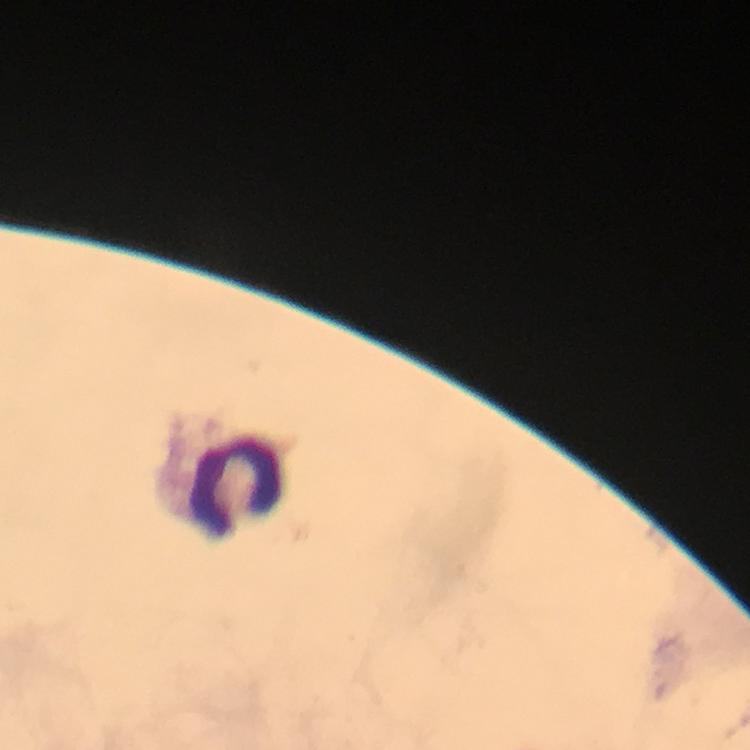
capture: smartphone camera through the microscope
immersion_oil: used
stain: Giemsa
leukocyte_locations: 'approximate centers as [x, y] in pixels: [235, 486]'
preparation: thick blood smear
image_size: 750×750 pixels
plasmodium_parasites: none seen
context: from a malaria diagnostic workup
cropped_from: one field of view
magnification: 100x